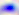

Summary:
  - Magnification: 400x
  - Modality: photomicrograph
  - Identification: Toxoplasma gondii